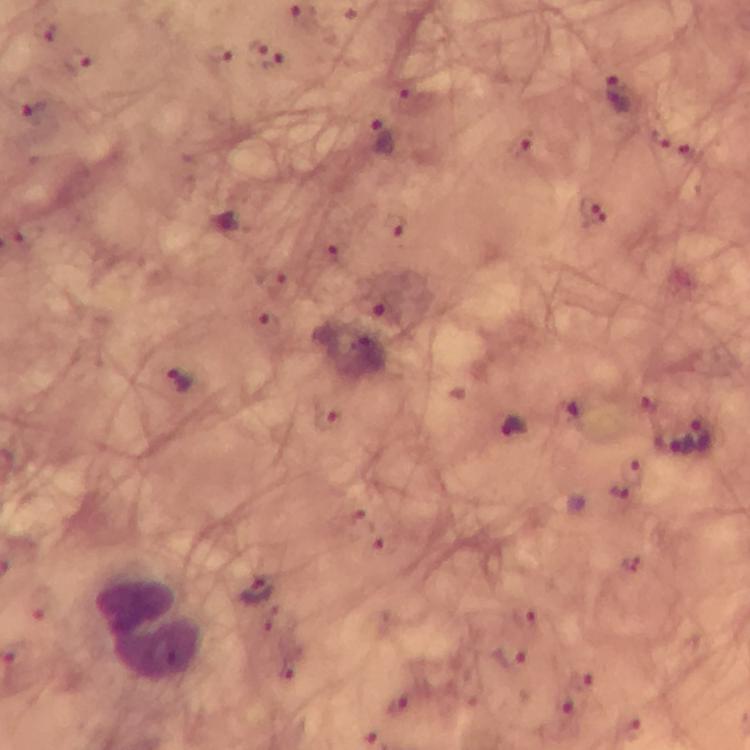
Approximate centers as [x, y] in pixels.
Summary:
  - Plasmodium parasite locations: [219, 51], [264, 54], [78, 60], [619, 92], [35, 113], [382, 137], [521, 145], [593, 211], [397, 225], [340, 258], [386, 312], [181, 382], [512, 426], [703, 434], [673, 443], [257, 590], [510, 660], [586, 679], [566, 706], [399, 707]
  - Leukocyte locations: [147, 631]
  - Context: from a malaria diagnostic workup
  - Immersion oil: applied
  - Preparation: thick blood film
  - Capture: smartphone camera through the microscope
  - Magnification: 100x
  - Stain: Giemsa
  - Cropped from: one field of view
  - Image size: 750×750 pixels